Outline every leukocyte.
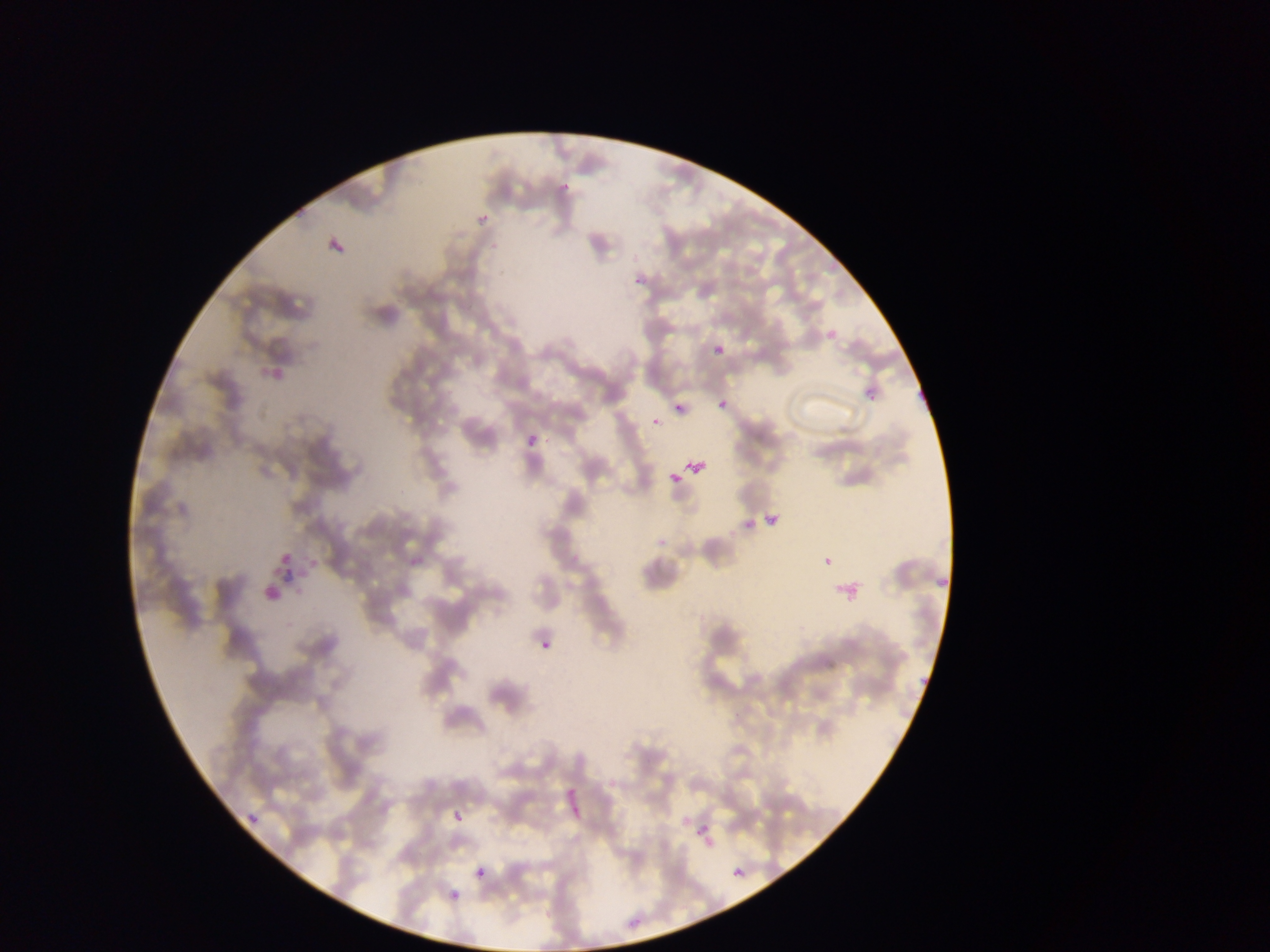

No leukocytes observed.

field of view = single
image size = 1270×952 pixels
Plasmodium parasite locations = approximate bounding boxes as [left, top, right, bottom] in pixels: [558, 182, 573, 199], [475, 210, 493, 229], [629, 276, 644, 287], [820, 324, 844, 350], [709, 340, 729, 361], [263, 354, 289, 388], [859, 380, 886, 410], [673, 391, 692, 414], [713, 398, 726, 407], [647, 403, 664, 424], [523, 432, 543, 455], [682, 454, 712, 483], [667, 469, 681, 484], [758, 506, 787, 535], [736, 513, 749, 530], [277, 543, 297, 566], [307, 550, 320, 572], [815, 551, 830, 567], [930, 564, 948, 586], [257, 567, 287, 602], [289, 567, 306, 585], [828, 577, 861, 606], [537, 634, 559, 659], [916, 664, 927, 683], [559, 770, 582, 823], [246, 800, 265, 825], [445, 801, 467, 826], [691, 821, 720, 853], [472, 864, 491, 884], [728, 864, 750, 885], [447, 876, 467, 899]
country = Ghana
capture = mobile-phone photograph through a microscope
preparation = thin blood smear